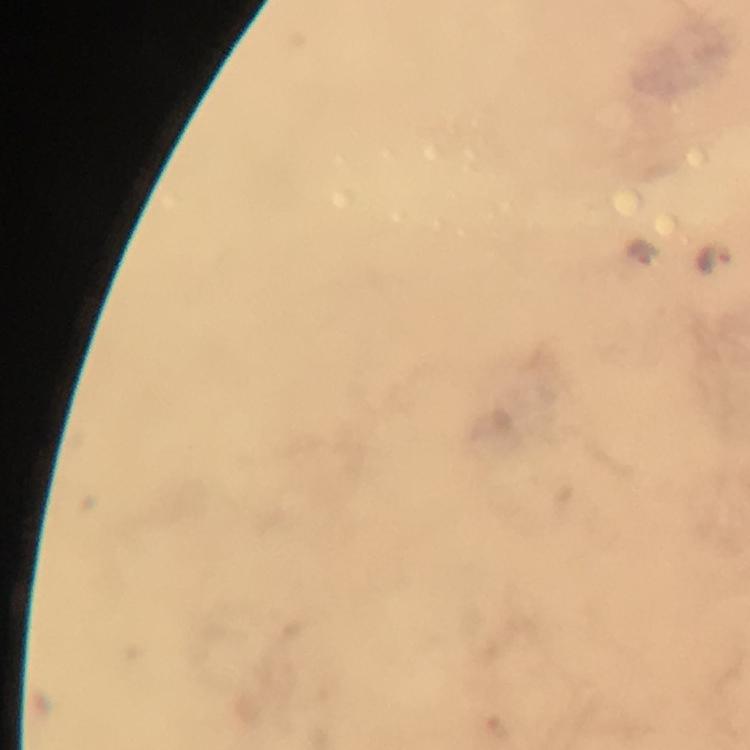

Approximate centers as (x, y) in pixels.
Summary:
  - Malaria parasite locations: (641, 254), (715, 260)
  - Image size: 750×750 pixels
  - Magnification: 100x
  - Stain: Giemsa
  - Capture: smartphone camera through the microscope
  - Cropped from: one field of view
  - Context: from a diagnostic examination for malaria
  - Preparation: thick blood film
  - Immersion oil: applied